Give the extent of all uninfected red blood cells.
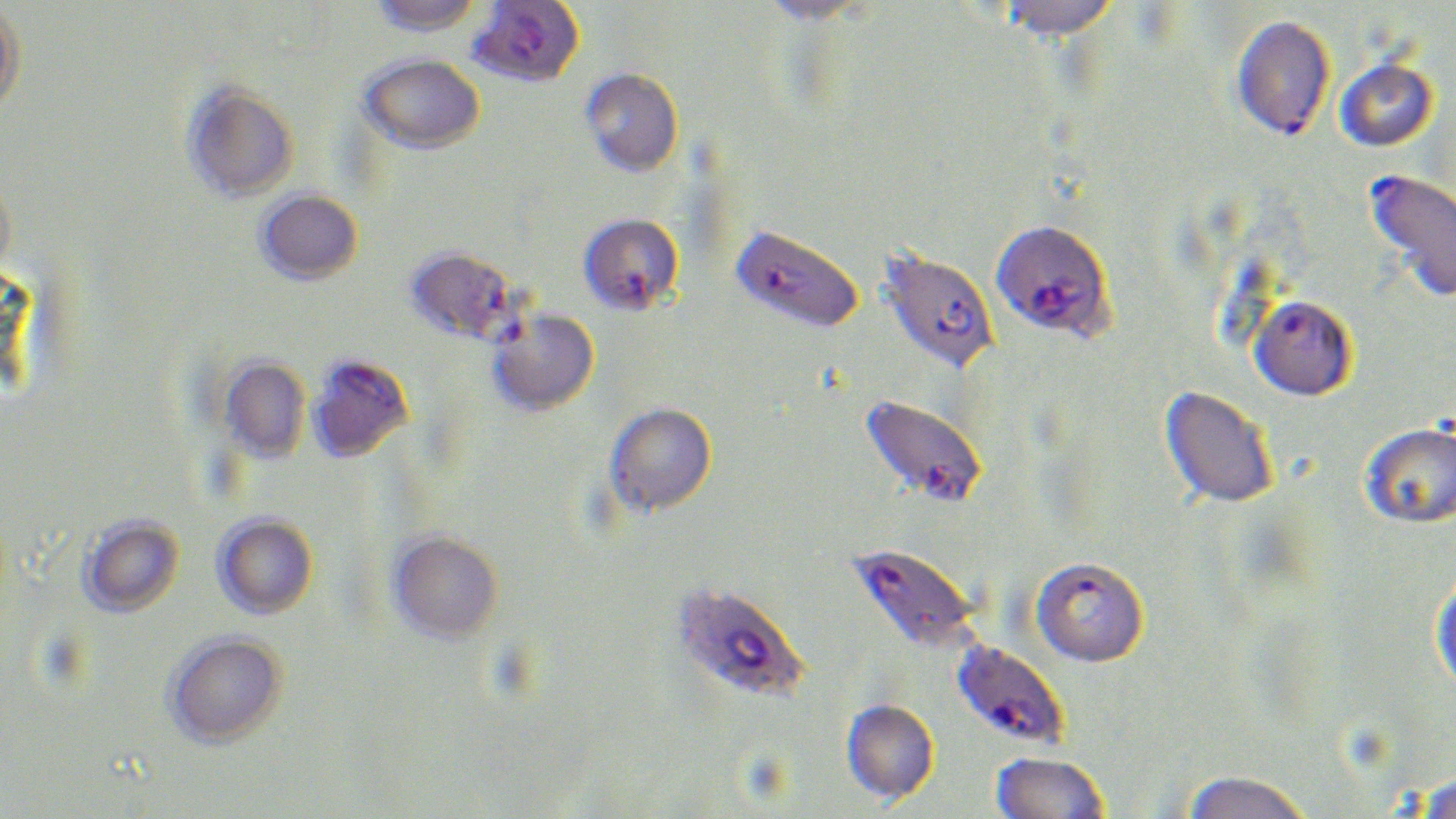
Approximate bounding boxes as named x1/y1/x2/y2 corners in pixels.
Uninfected red blood cells: (x1=369, y1=0, x2=484, y2=36), (x1=753, y1=0, x2=880, y2=26), (x1=996, y1=0, x2=1121, y2=43), (x1=0, y1=2, x2=26, y2=114), (x1=358, y1=52, x2=485, y2=153), (x1=1335, y1=58, x2=1439, y2=151), (x1=580, y1=67, x2=683, y2=176), (x1=182, y1=81, x2=299, y2=202), (x1=0, y1=178, x2=16, y2=281), (x1=256, y1=189, x2=363, y2=285), (x1=220, y1=356, x2=311, y2=464), (x1=1158, y1=386, x2=1278, y2=509), (x1=604, y1=402, x2=717, y2=517), (x1=1359, y1=421, x2=1456, y2=529), (x1=212, y1=513, x2=319, y2=619), (x1=79, y1=515, x2=185, y2=617), (x1=388, y1=531, x2=503, y2=644), (x1=1429, y1=577, x2=1456, y2=699), (x1=165, y1=631, x2=287, y2=748), (x1=840, y1=700, x2=940, y2=806), (x1=990, y1=753, x2=1109, y2=819), (x1=1181, y1=772, x2=1314, y2=819), (x1=1414, y1=773, x2=1455, y2=819).

Summary:
  - Plasmodium falciparum-infected red blood cell locations: (x1=469, y1=1, x2=586, y2=88), (x1=1231, y1=14, x2=1336, y2=141), (x1=1363, y1=168, x2=1456, y2=304), (x1=578, y1=212, x2=685, y2=317), (x1=989, y1=221, x2=1116, y2=344), (x1=735, y1=231, x2=862, y2=336), (x1=406, y1=245, x2=520, y2=343), (x1=876, y1=247, x2=999, y2=376), (x1=1249, y1=297, x2=1356, y2=402), (x1=487, y1=308, x2=600, y2=415), (x1=308, y1=353, x2=415, y2=463), (x1=859, y1=394, x2=988, y2=510), (x1=848, y1=544, x2=981, y2=653), (x1=1029, y1=559, x2=1149, y2=670), (x1=672, y1=582, x2=809, y2=703), (x1=955, y1=641, x2=1068, y2=755)
  - Slide-level diagnosis: Plasmodium falciparum
  - Preparation: thin blood film
  - Field of view: single
  - Modality: optical microscopy
  - Image size: 1456×819 pixels
  - Stain: May-Grünwald-Giemsa
  - Magnification: 1000x